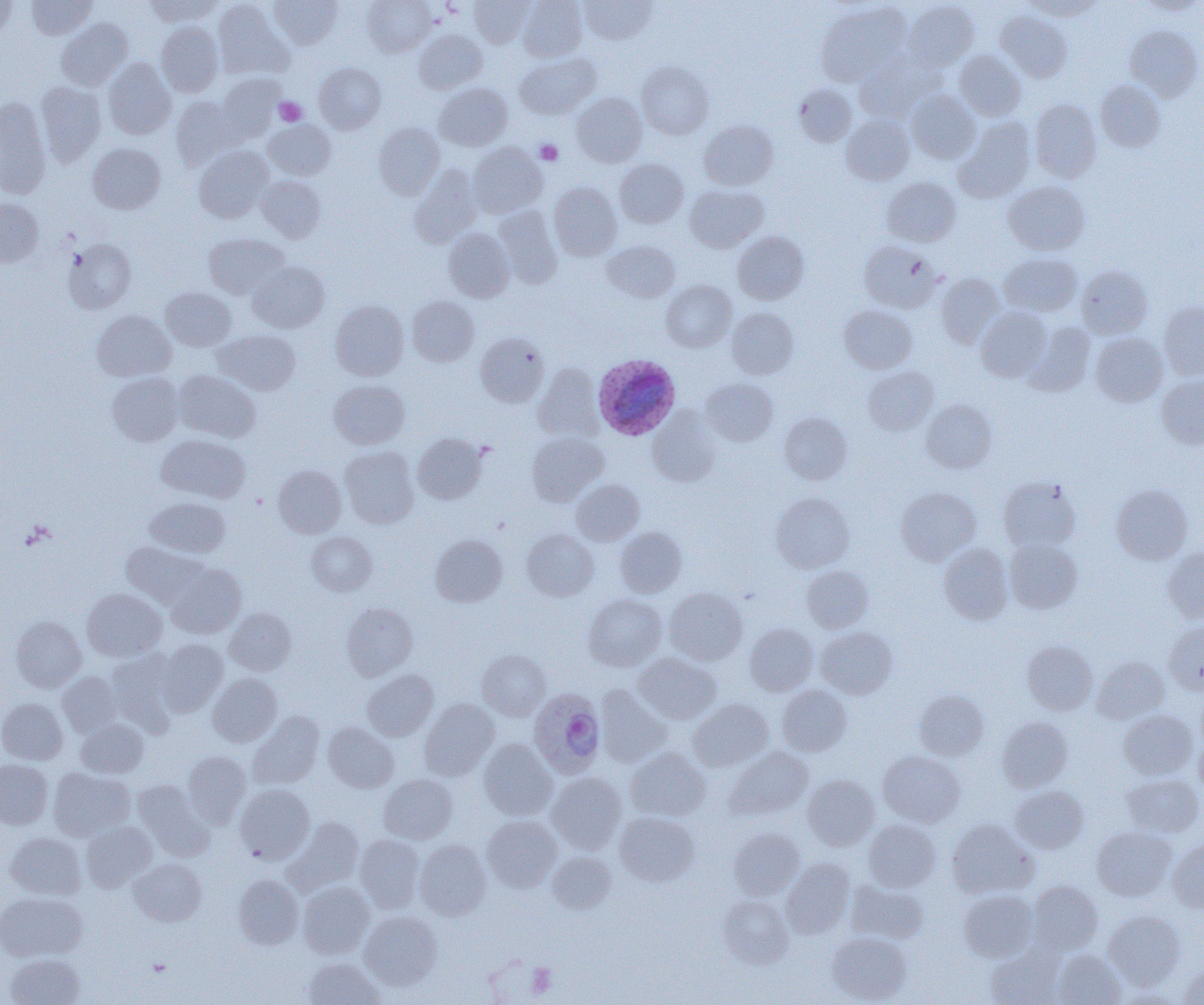

Approximate bounding boxes as [x1, y1, x2, y2] in pixels. Plasmodium ovale-infected red blood cell locations: [593, 354, 681, 440], [528, 688, 606, 778]. Uninfected red blood cell locations: [26, 0, 97, 39], [145, 0, 221, 25], [269, 0, 342, 49], [362, 0, 436, 56], [470, 0, 533, 47], [518, 0, 587, 61], [579, 0, 658, 44], [1021, 0, 1100, 20], [0, 1, 17, 39], [213, 1, 291, 78], [904, 1, 979, 71], [1139, 1, 1203, 16], [816, 2, 912, 86], [995, 10, 1072, 83], [56, 18, 132, 90], [155, 22, 223, 97], [1126, 25, 1203, 101], [415, 29, 487, 93], [955, 51, 1026, 121], [515, 53, 600, 119], [854, 55, 935, 123], [103, 58, 175, 139], [636, 61, 714, 139], [315, 63, 386, 134], [217, 74, 285, 140], [36, 81, 105, 166], [1095, 81, 1165, 152], [434, 83, 512, 151], [794, 84, 857, 146], [906, 91, 980, 163], [572, 92, 647, 166], [170, 96, 243, 168], [0, 97, 51, 198], [1029, 99, 1101, 182], [841, 114, 915, 184], [955, 118, 1034, 202], [264, 120, 337, 179], [699, 120, 777, 190], [373, 123, 444, 199], [88, 143, 166, 214], [468, 143, 546, 217], [194, 146, 273, 223], [615, 158, 689, 228], [410, 165, 482, 247], [257, 175, 326, 242], [881, 177, 961, 246], [1004, 181, 1089, 255], [548, 182, 622, 260], [685, 185, 767, 252], [0, 198, 43, 266], [494, 206, 562, 288], [443, 228, 515, 302], [732, 231, 809, 304], [204, 233, 289, 299], [63, 239, 136, 314], [602, 241, 680, 302], [859, 241, 940, 312], [999, 253, 1082, 316], [248, 261, 329, 333], [1076, 265, 1152, 338], [936, 272, 1005, 347], [661, 279, 736, 351], [161, 288, 236, 351], [408, 295, 479, 366], [330, 300, 409, 380], [1159, 300, 1204, 379], [839, 305, 917, 373], [727, 307, 799, 379], [976, 307, 1052, 382], [92, 310, 175, 381], [1025, 322, 1095, 395], [214, 330, 301, 395], [475, 332, 549, 407], [1090, 332, 1168, 406], [533, 363, 603, 441], [862, 365, 938, 435], [174, 370, 260, 442], [107, 373, 183, 446], [1156, 374, 1204, 449], [701, 377, 778, 446], [328, 379, 410, 449], [921, 399, 997, 473], [648, 409, 721, 486], [779, 412, 851, 484], [527, 431, 608, 504], [413, 433, 486, 504], [156, 434, 250, 503], [340, 446, 419, 528], [273, 465, 346, 538], [998, 478, 1080, 553], [572, 480, 644, 545], [1111, 484, 1193, 565], [896, 487, 981, 565], [770, 492, 855, 573], [145, 497, 230, 558], [615, 527, 687, 597], [522, 529, 598, 601], [307, 531, 377, 596], [431, 534, 508, 606], [1004, 538, 1082, 613], [122, 542, 208, 609], [939, 544, 1013, 624], [1163, 547, 1204, 623], [166, 564, 245, 638], [801, 565, 873, 633], [665, 587, 748, 665], [82, 588, 166, 661], [584, 594, 666, 670], [341, 602, 418, 680], [225, 608, 296, 675], [11, 616, 86, 691], [1164, 620, 1204, 694], [745, 624, 818, 696], [816, 626, 897, 699], [156, 639, 229, 715], [1022, 641, 1097, 715], [107, 648, 181, 732], [477, 649, 551, 720], [634, 652, 721, 724], [1091, 656, 1169, 723], [362, 669, 438, 740], [58, 672, 122, 736], [207, 673, 283, 747], [777, 685, 852, 756], [595, 686, 671, 767], [914, 689, 989, 760], [0, 698, 67, 764], [688, 698, 773, 771], [419, 699, 498, 780], [1119, 709, 1197, 779], [249, 711, 325, 789], [997, 716, 1073, 792], [77, 718, 148, 778], [323, 722, 398, 792], [1194, 737, 1204, 801], [479, 739, 557, 820], [726, 747, 813, 821], [626, 748, 710, 821], [183, 751, 251, 827], [878, 751, 965, 827], [0, 759, 52, 829], [49, 767, 135, 841], [547, 772, 627, 853], [1122, 773, 1203, 837], [379, 774, 457, 844], [803, 775, 879, 850], [132, 780, 209, 856], [235, 784, 315, 864], [1011, 785, 1088, 853], [615, 811, 700, 885], [482, 815, 562, 892], [284, 817, 364, 894], [946, 818, 1038, 898], [863, 819, 940, 891], [81, 821, 157, 891], [1092, 826, 1176, 901], [729, 827, 804, 900], [5, 833, 86, 899], [355, 835, 425, 912], [414, 839, 490, 919], [1168, 840, 1204, 912], [548, 851, 617, 913], [782, 857, 855, 937], [128, 859, 206, 926], [234, 875, 303, 949], [298, 881, 374, 958], [847, 881, 929, 944], [1027, 881, 1103, 955], [959, 889, 1038, 962], [0, 892, 87, 961], [718, 895, 794, 968], [359, 910, 442, 990], [1103, 910, 1186, 990], [827, 931, 911, 1003], [985, 945, 1066, 1005], [1053, 949, 1126, 1005], [4, 953, 85, 1005], [303, 957, 384, 1004], [1178, 963, 1204, 1004]. Platelet locations: [274, 97, 306, 126], [535, 140, 562, 164], [527, 963, 557, 996]. Slide-level diagnosis: Plasmodium ovale. Light microscopy. 1000x magnification. Thin blood smear. Image is 1204×1005 pixels. One field of a larger specimen.